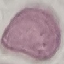
result = negative for malaria parasites
capture = smartphone camera at the microscope eyepiece
image type = cell patch, automatically extracted from a larger field of view and resized to 64 × 64 pixels
preparation = thin smear
stain = Giemsa